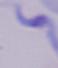 Photomicrograph. A trypanosome is seen. Captured at 1000x magnification.